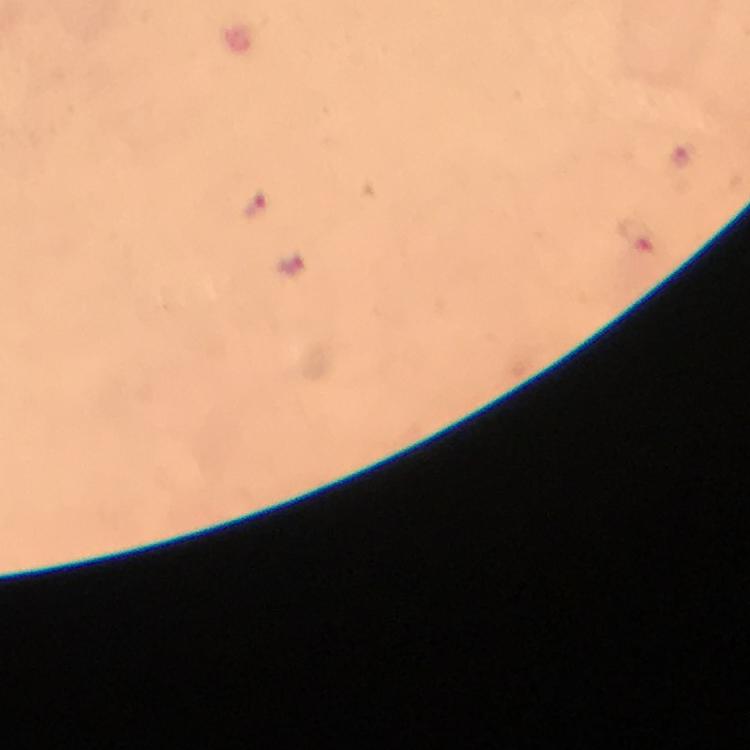
Approximate centers as {x, y} in pixels. Plasmodium parasite locations: {255, 206}, {638, 235}, {294, 270}. From a diagnostic examination for malaria. Thick blood film. 100x magnification. Image is 750×750 pixels. Cropped region of a single field of view. Photographed with a smartphone mounted on the microscope. Immersion oil was used. Giemsa stain.